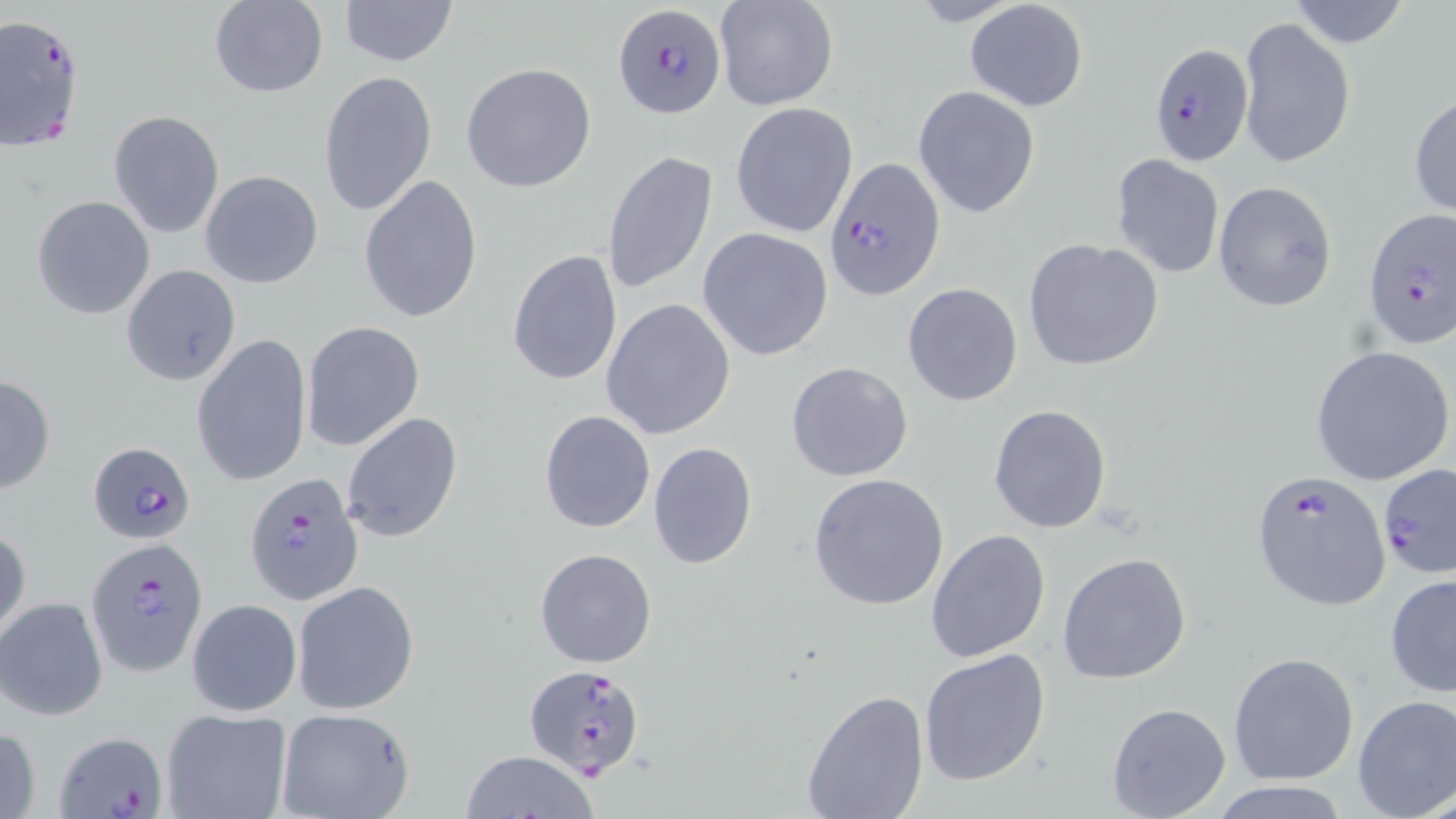

Approximate bounding boxes as (x1, y1, x2, y2) in pixels. Uninfected red blood cell locations: (338, 0, 459, 66), (714, 0, 838, 112), (963, 0, 1089, 112), (1285, 0, 1413, 50), (209, 1, 327, 98), (1237, 16, 1355, 168), (461, 61, 599, 194), (316, 70, 436, 221), (913, 85, 1041, 218), (1410, 92, 1456, 221), (730, 103, 858, 237), (107, 110, 225, 239), (603, 148, 717, 294), (1111, 154, 1225, 278), (200, 171, 325, 290), (358, 173, 485, 324), (1212, 181, 1337, 312), (32, 195, 156, 321), (697, 227, 837, 361), (1023, 238, 1164, 370), (505, 248, 623, 386), (121, 264, 241, 387), (902, 282, 1024, 406), (600, 298, 735, 441), (300, 320, 424, 452), (192, 334, 313, 486), (1311, 345, 1455, 487), (786, 361, 913, 482), (0, 376, 55, 495), (988, 404, 1112, 533), (538, 410, 654, 533), (341, 411, 463, 543), (647, 442, 758, 569), (807, 473, 951, 611), (0, 524, 30, 644), (926, 530, 1051, 663), (534, 548, 657, 667), (1058, 553, 1192, 685), (1385, 574, 1456, 700), (293, 581, 419, 716), (0, 597, 107, 720), (186, 598, 302, 716), (918, 648, 1052, 787), (1228, 652, 1359, 786), (800, 688, 931, 819), (1351, 695, 1456, 819), (1106, 701, 1231, 819), (159, 707, 292, 819), (276, 710, 416, 819), (1, 722, 42, 819), (463, 750, 597, 819), (1210, 782, 1353, 818). Plasmodium falciparum-infected red blood cell locations: (611, 2, 726, 120), (0, 14, 86, 150), (1147, 42, 1255, 166), (826, 159, 945, 298), (1362, 210, 1455, 351), (87, 441, 193, 544), (1378, 463, 1455, 578), (1251, 471, 1392, 608), (243, 472, 362, 606), (86, 535, 208, 676), (523, 663, 650, 784), (57, 731, 170, 819). Slide-level diagnosis: Plasmodium falciparum. Thin blood smear. May-Grünwald-Giemsa-stained preparation. Image is 1456×819 pixels. Light microscopy. One field of a larger specimen. 1000x magnification.